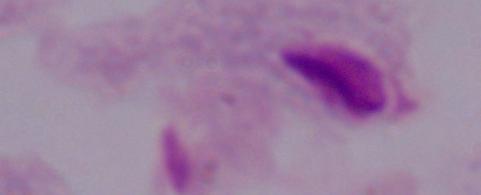
{
  "identification": "trichomonad",
  "modality": "photomicrograph",
  "magnification": "1000x"
}